Locate and identify every blood parasite.
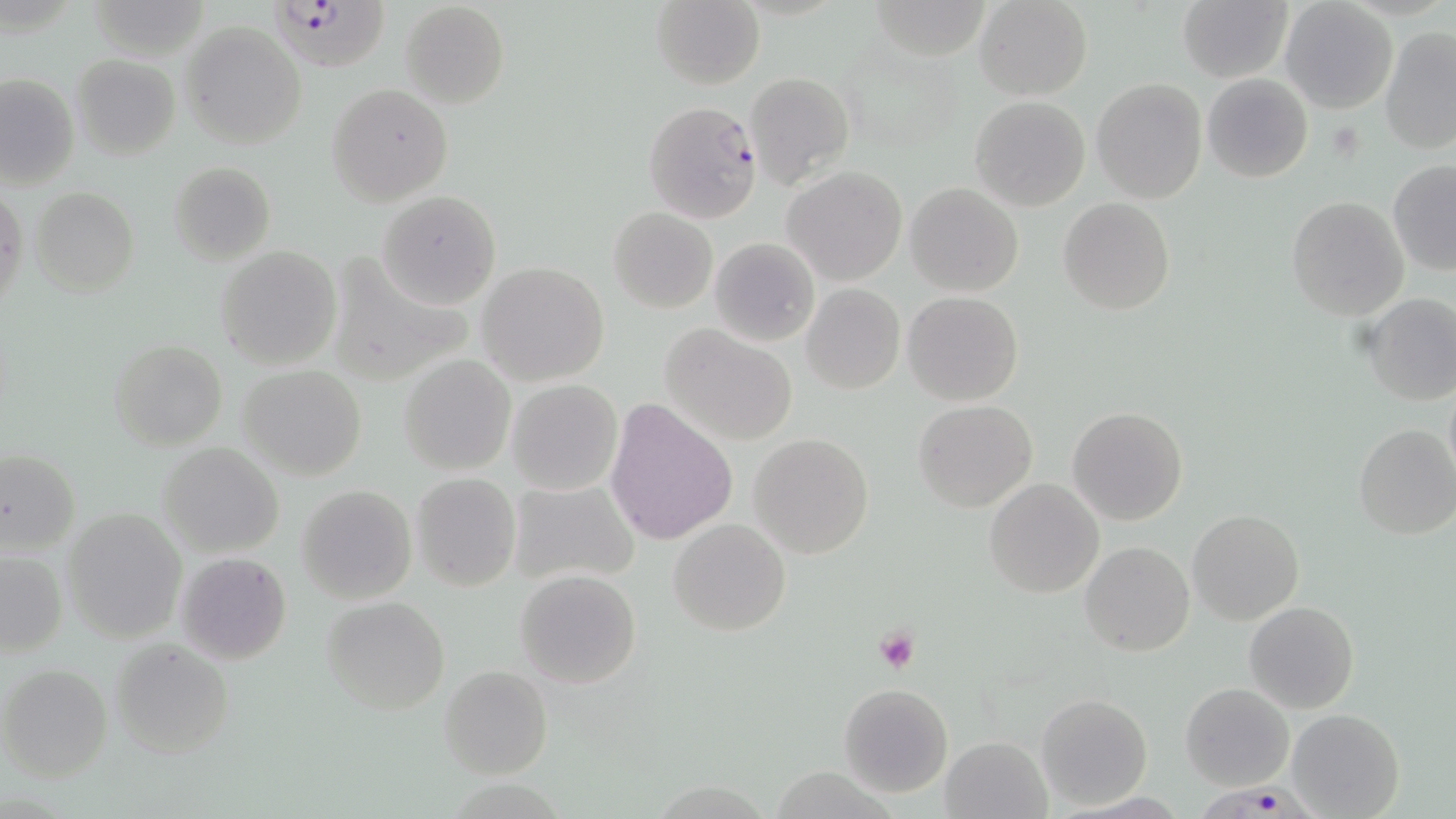
Approximate bounding boxes as [x1, y1, x2, y2] in pixels.
Plasmodium falciparum-infected red blood cells: [263, 0, 399, 75], [1199, 776, 1319, 819].
No Plasmodium ovale, Plasmodium malariae, Plasmodium vivax, Babesia divergens, or Trypanosoma brucei observed.

Platelet locations: [874, 627, 919, 675]. Uninfected red blood cell locations: [861, 0, 989, 62], [974, 0, 1092, 100], [400, 1, 509, 109], [650, 1, 764, 88], [1177, 1, 1293, 83], [1280, 1, 1397, 113], [181, 21, 306, 150], [1380, 27, 1456, 154], [71, 52, 180, 159], [744, 71, 854, 189], [1, 74, 78, 188], [1202, 74, 1314, 183], [1091, 79, 1208, 204], [326, 82, 453, 206], [969, 95, 1091, 211], [643, 101, 762, 223], [1387, 160, 1456, 273], [168, 161, 276, 265], [783, 166, 907, 285], [904, 183, 1024, 297], [33, 187, 138, 296], [1, 188, 25, 312], [377, 190, 502, 309], [1286, 196, 1409, 321], [1058, 197, 1175, 316], [609, 208, 717, 313], [710, 237, 820, 348], [216, 247, 341, 369], [324, 251, 474, 384], [478, 262, 609, 387], [801, 283, 905, 394], [903, 291, 1023, 406], [1361, 292, 1455, 406], [660, 323, 798, 445], [109, 340, 228, 450], [398, 355, 516, 475], [238, 366, 367, 481], [506, 380, 623, 495], [913, 400, 1038, 511], [606, 401, 737, 545], [1066, 407, 1188, 526], [1353, 424, 1456, 539], [748, 433, 874, 558], [157, 442, 285, 558], [0, 451, 81, 553], [412, 473, 520, 591], [506, 478, 639, 588], [985, 479, 1104, 600], [297, 484, 416, 604], [62, 508, 187, 643], [1186, 508, 1304, 624], [668, 518, 791, 636], [1081, 542, 1194, 657], [0, 548, 68, 660], [176, 552, 292, 665], [515, 569, 642, 689], [321, 597, 450, 715], [1245, 600, 1359, 714], [110, 638, 235, 758], [1, 664, 113, 782], [440, 665, 552, 779], [1180, 682, 1294, 789], [838, 683, 952, 797], [1036, 694, 1152, 810], [1286, 709, 1405, 819], [940, 735, 1049, 818], [776, 761, 901, 819]. Slide-level diagnosis: Plasmodium falciparum. May-Grünwald-Giemsa-stained preparation. Image is 1456×819 pixels. 1000x magnification. Thin blood smear. One field of a larger specimen. Optical microscopy.